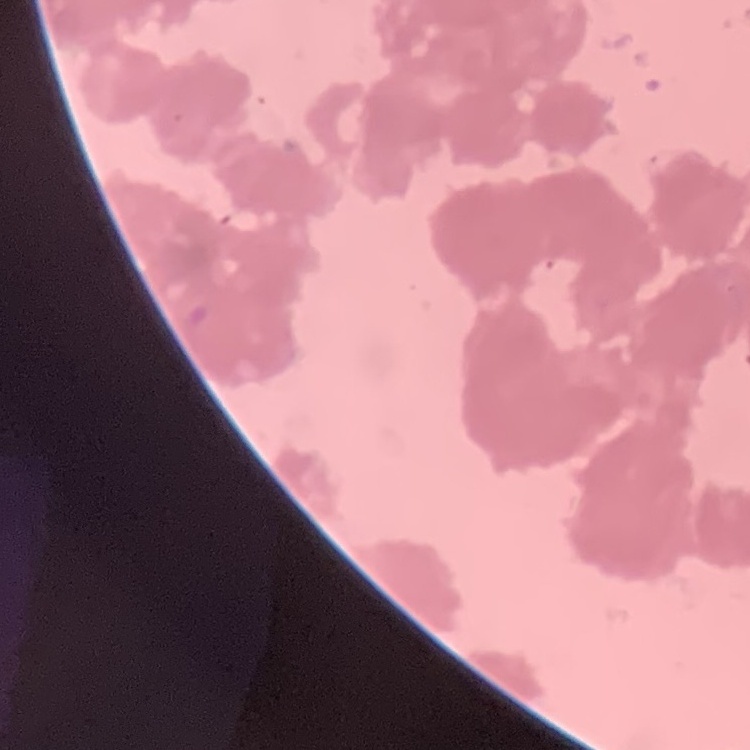

red blood cell morphology = rouleaux formation
stain = Field's or Giemsa
preparation = thin blood smear
image type = square crop of a larger photomicrograph